Give the position of every Plasmodium parasite visible.
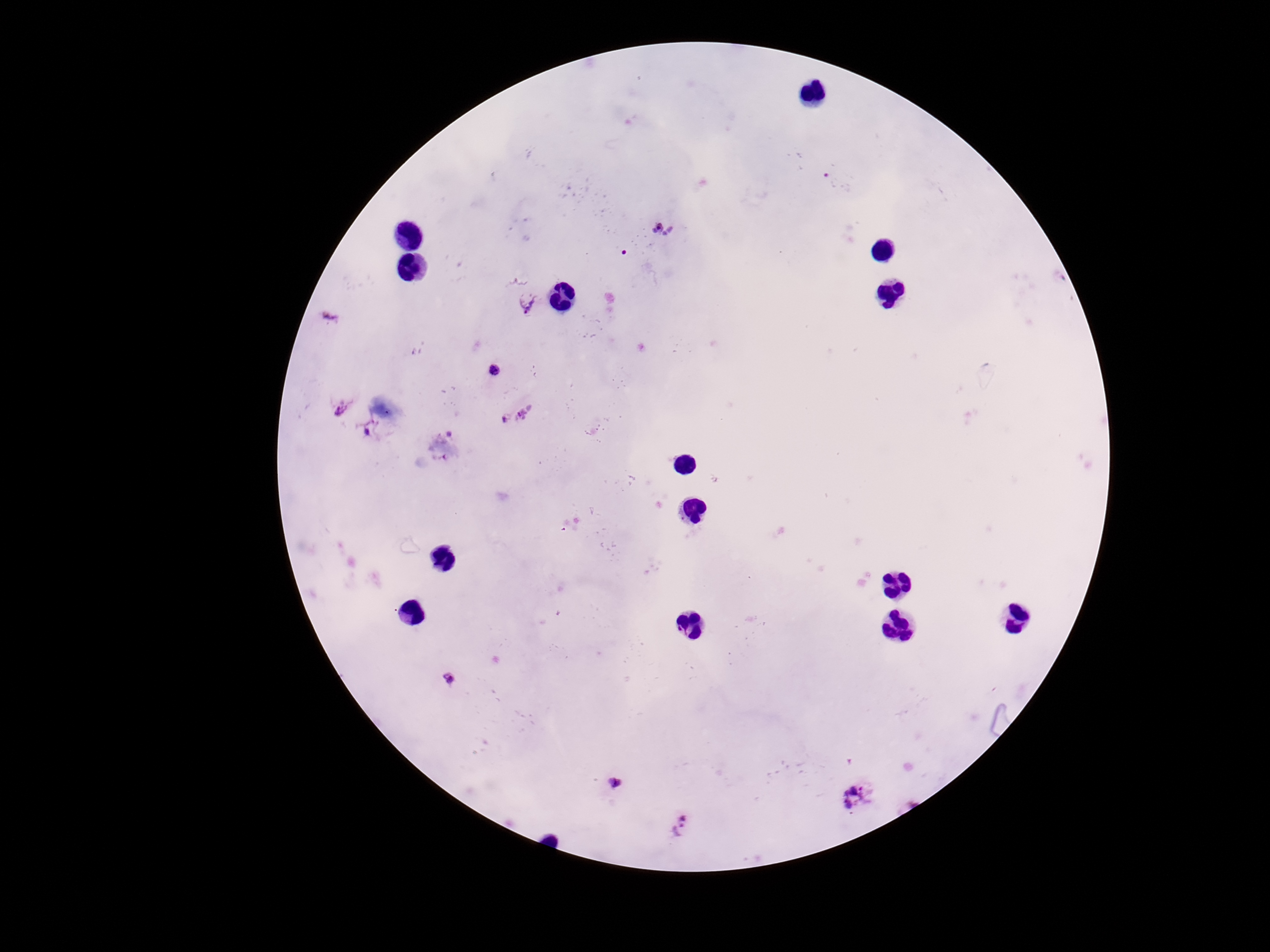
Approximate centers as {x, y} in pixels.
Plasmodium parasites: {661, 230}, {527, 302}, {332, 318}, {494, 371}, {342, 408}, {517, 416}, {371, 430}, {450, 679}, {613, 785}, {856, 794}, {682, 826}.

Summary:
  - Field of view: single
  - Image size: 1270×952 pixels
  - Stain: Giemsa
  - Preparation: thick blood smear
  - Patient malaria status: infected
  - Capture: smartphone camera through the microscope eyepiece
  - Magnification: 100x